Classify this cell by malaria status.
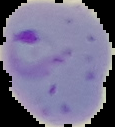

It is parasitized.

Summary:
  - Image type: segmented cell region with the area outside set to black
  - Preparation: thin blood smear
  - Image size: 115×127 pixels